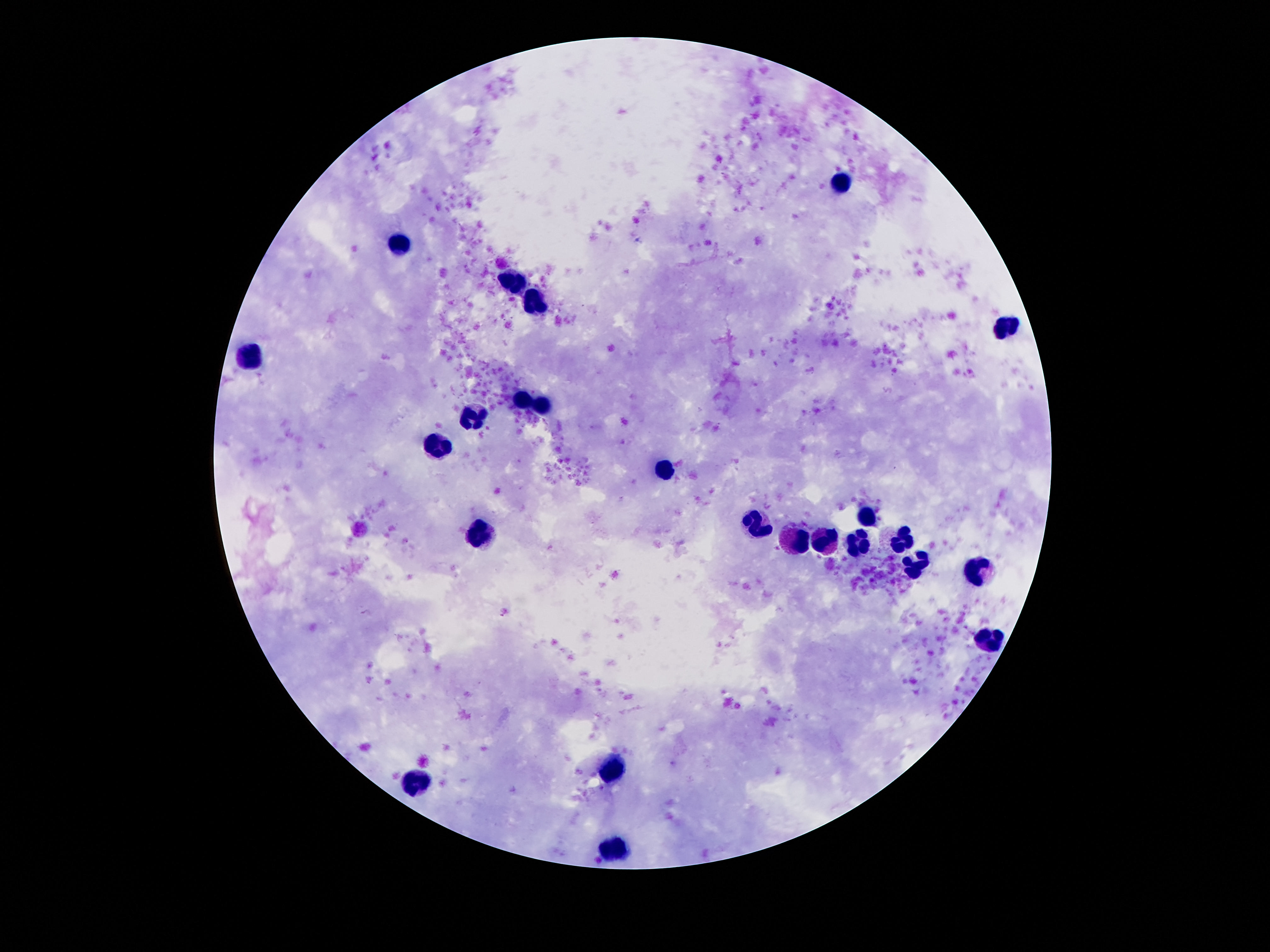

Approximate centers as (x, y) in pixels.
Summary:
  - Leukocyte locations: (842, 183), (400, 245), (513, 283), (536, 306), (1006, 327), (253, 354), (523, 402), (542, 407), (473, 421), (437, 451), (666, 473), (868, 516), (760, 522), (483, 537), (903, 540), (792, 542), (857, 542), (825, 543), (914, 566), (983, 575), (993, 638), (616, 768), (420, 783), (614, 848)
  - Magnification: 100x
  - Preparation: thick peripheral-blood smear
  - Capture: smartphone camera through the microscope eyepiece
  - Image size: 1270×952 pixels
  - Field of view: one from this slide
  - Stain: Giemsa
  - Patient malaria status: negative